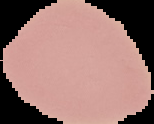

Summary:
  - Image size: 154×124 pixels
  - Preparation: thin blood film
  - Image type: segmented cell region on a black background
  - Result: no Plasmodium parasites detected